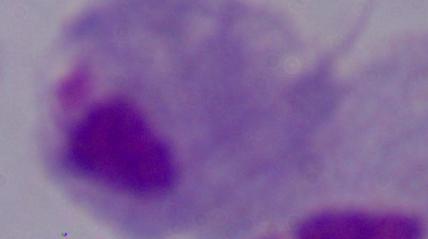
Summary:
  - Identification: trichomonad
  - Magnification: 1000x
  - Modality: micrograph